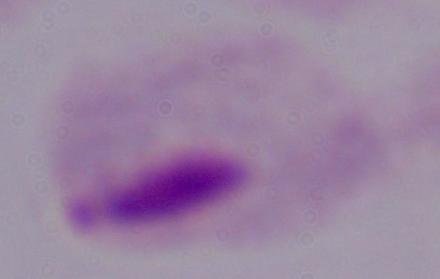
Summary:
  - Magnification: 1000x
  - Modality: micrograph
  - Identification: trichomonad